Report the malaria status of this cell.
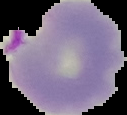

Parasitized.

The area outside the segmented cell region is set to black. From a thin blood smear. Image is 127×115 pixels.